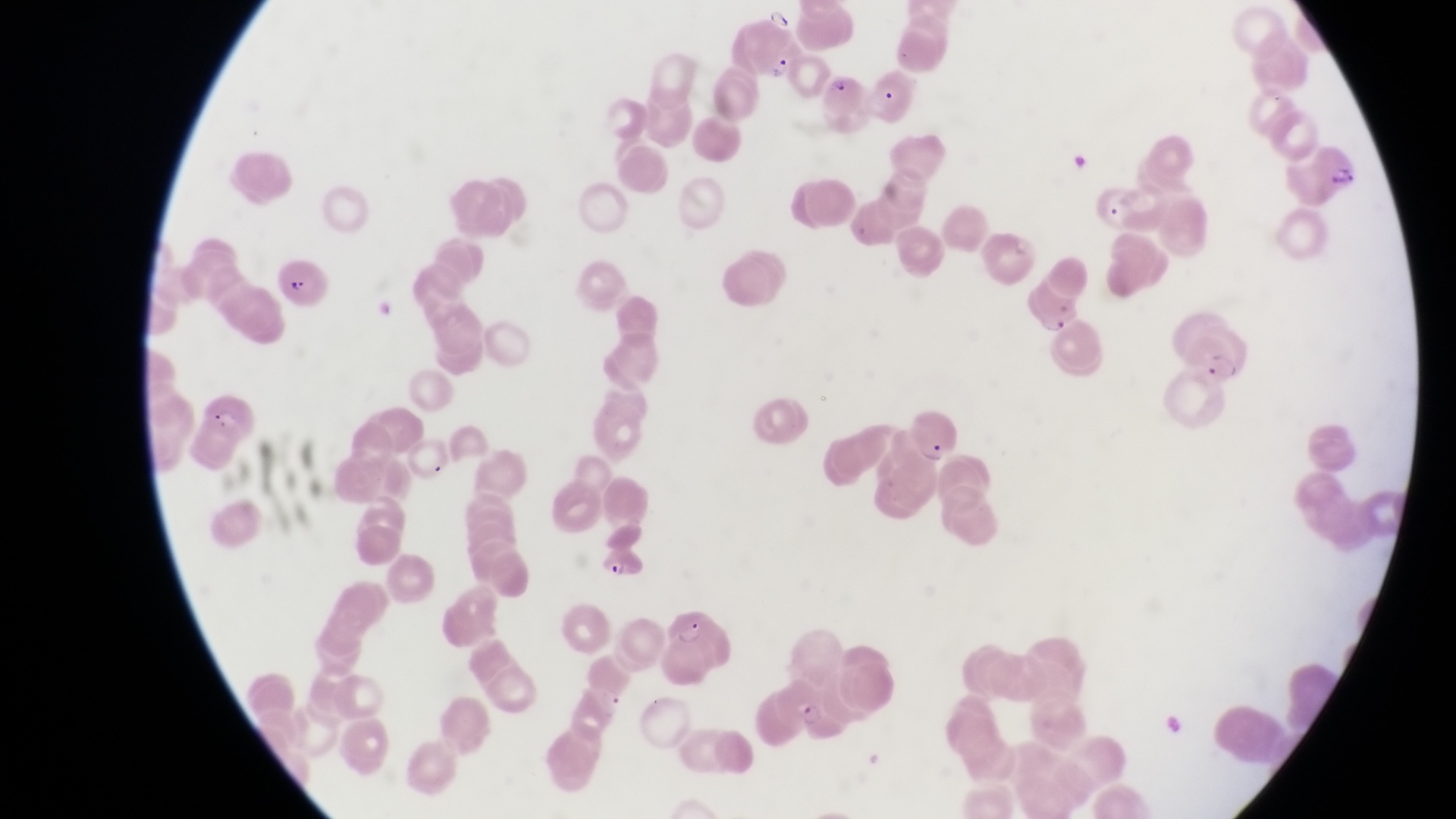

Approximate bounding boxes as [left, top, right, bottom] in pixels. Trophozoite locations: [800, 701, 827, 734]. Parasitised red blood cell locations: [750, 37, 806, 86], [825, 72, 871, 125], [1304, 138, 1365, 199], [1097, 174, 1146, 233], [279, 259, 325, 313], [1023, 277, 1082, 333], [1184, 334, 1248, 407], [198, 394, 261, 447], [911, 400, 960, 467], [602, 536, 648, 585], [660, 611, 742, 684]. Image is 1456×819 pixels. Sample from Uganda. Thin blood smear. Single field of view. Photographed through the eyepiece of an Olympus CX-23 microscope with a smartphone camera. Magnification of 1000x.